Locate and identify every blood parasite.
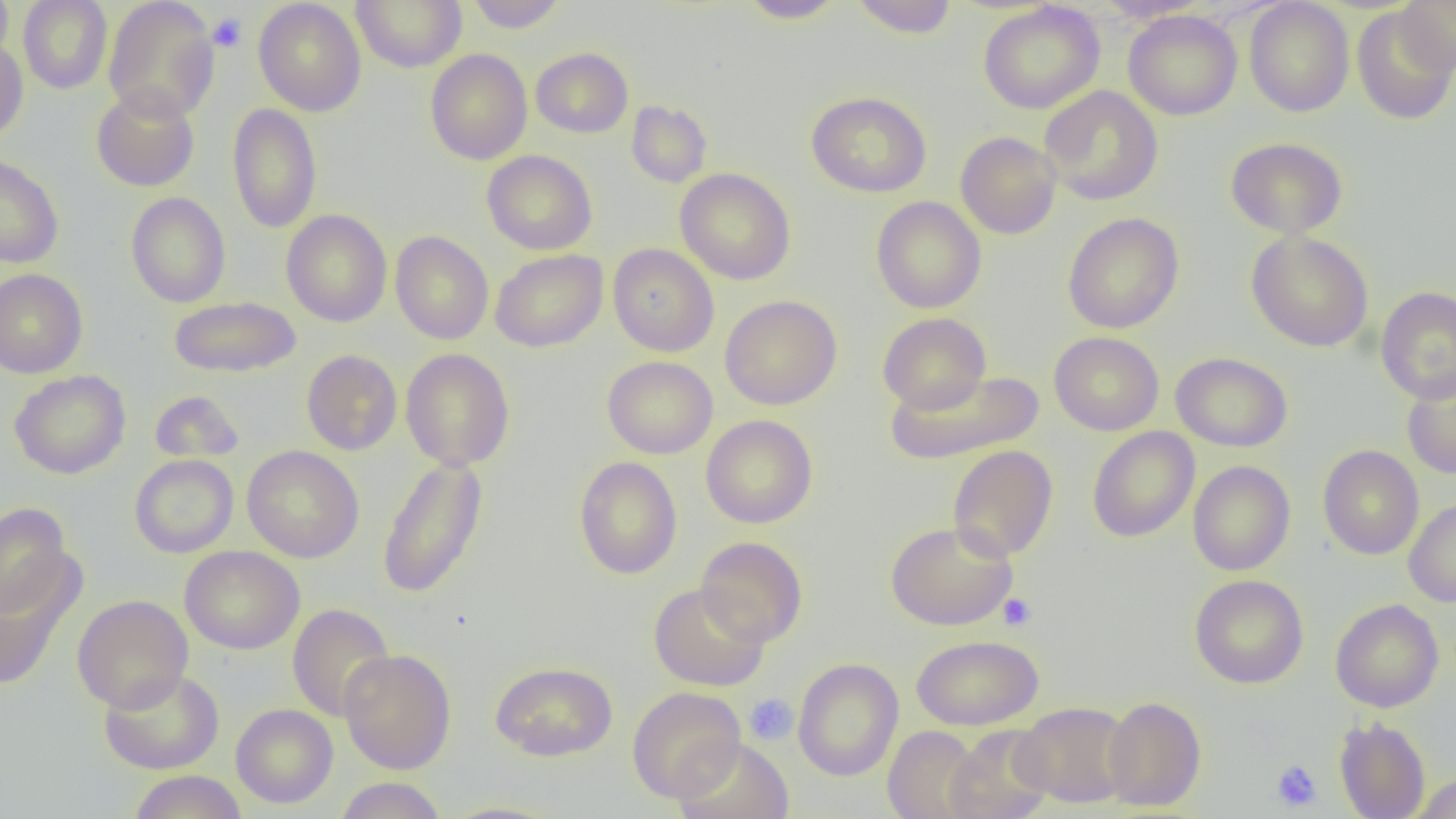
No blood parasites seen.

slide_level_diagnosis: negative for blood parasites
field_of_view: one of a larger specimen
image_size: 1456×819 pixels
uninfected_red_blood_cell_locations: 'approximate bounding boxes as (x1, y1, x2, y2) in pixels: (0, 0, 14, 70), (18, 0, 112, 94), (253, 0, 366, 117), (351, 0, 467, 72), (465, 0, 567, 33), (737, 0, 848, 23), (850, 0, 959, 39), (1094, 0, 1211, 22), (1244, 0, 1354, 117), (1396, 0, 1456, 74), (103, 1, 219, 122), (977, 2, 1105, 114), (1351, 4, 1456, 126), (1123, 10, 1242, 121), (0, 37, 28, 144), (531, 47, 633, 138), (425, 49, 532, 165), (91, 86, 200, 191), (1040, 86, 1163, 205), (806, 91, 932, 197), (626, 100, 712, 188), (227, 102, 323, 233), (955, 131, 1062, 239), (1225, 136, 1348, 238), (482, 150, 597, 255), (0, 153, 64, 268), (675, 168, 796, 285), (126, 192, 230, 308), (871, 196, 986, 314), (280, 209, 392, 327), (1063, 213, 1184, 334), (390, 230, 493, 345), (1246, 231, 1374, 352), (608, 243, 719, 356), (490, 249, 608, 352), (0, 269, 88, 378), (1375, 286, 1456, 403), (720, 295, 842, 410), (168, 296, 302, 378), (877, 312, 992, 413), (1049, 332, 1164, 436), (400, 348, 515, 471), (301, 350, 402, 455), (1171, 352, 1293, 452), (602, 356, 718, 459), (884, 369, 1046, 465), (1401, 369, 1456, 481), (9, 370, 130, 479), (149, 390, 245, 464), (701, 414, 818, 528), (1087, 427, 1200, 542), (242, 445, 364, 563), (947, 445, 1058, 562), (1317, 445, 1424, 560), (1087, 448, 1294, 558), (129, 455, 238, 558), (376, 456, 489, 599), (573, 456, 683, 579), (1188, 460, 1295, 576), (1403, 498, 1456, 607), (0, 502, 74, 619), (885, 521, 1017, 631), (695, 536, 807, 647), (179, 546, 305, 654), (0, 560, 86, 691), (1189, 574, 1309, 689), (649, 582, 770, 691), (72, 594, 193, 713), (1330, 598, 1444, 713), (288, 603, 395, 722), (911, 635, 1044, 730), (339, 649, 456, 774), (792, 658, 903, 781), (490, 661, 618, 761), (98, 668, 224, 774), (627, 686, 745, 803), (1102, 696, 1207, 811), (1013, 702, 1132, 808), (231, 703, 338, 808), (1334, 717, 1431, 819), (883, 725, 985, 819), (944, 726, 1054, 819), (673, 737, 794, 819), (128, 770, 247, 819), (1409, 773, 1456, 819), (334, 776, 447, 818), (436, 801, 568, 819)'
preparation: thin blood film
platelet_locations: 'approximate bounding boxes as (x1, y1, x2, y2) in pixels: (208, 13, 247, 52), (998, 593, 1037, 631), (744, 693, 798, 745), (1270, 759, 1322, 812)'
magnification: 1000x
modality: optical microscopy